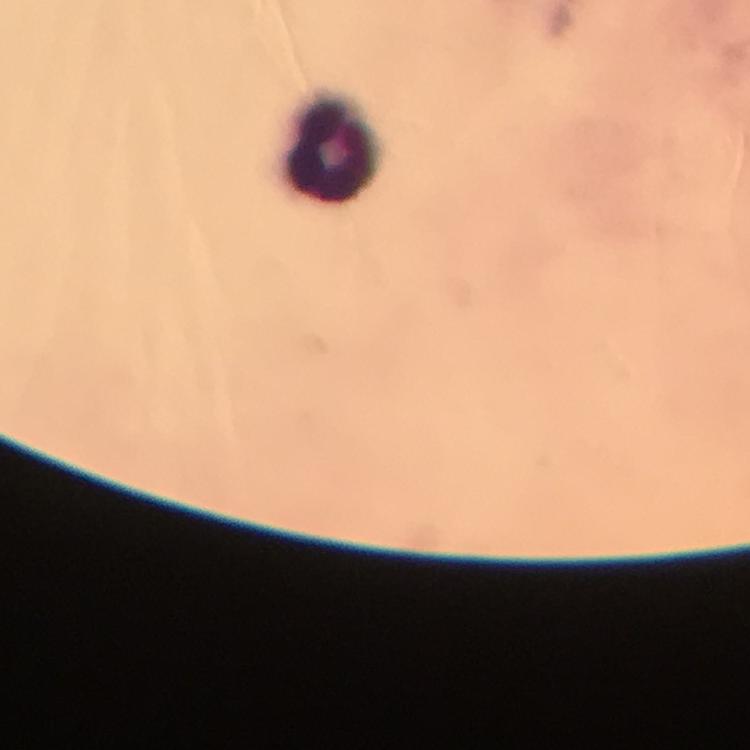
Approximate centers as {x, y} in pixels.
Summary:
  - Leukocyte locations: {331, 146}
  - Capture: smartphone photograph through a microscope
  - Context: from a diagnostic examination for malaria
  - Preparation: thick blood film
  - Immersion oil: applied
  - Cropped from: one field of view
  - Magnification: 100x
  - Malaria parasites: none detected
  - Image size: 750×750 pixels
  - Stain: Giemsa